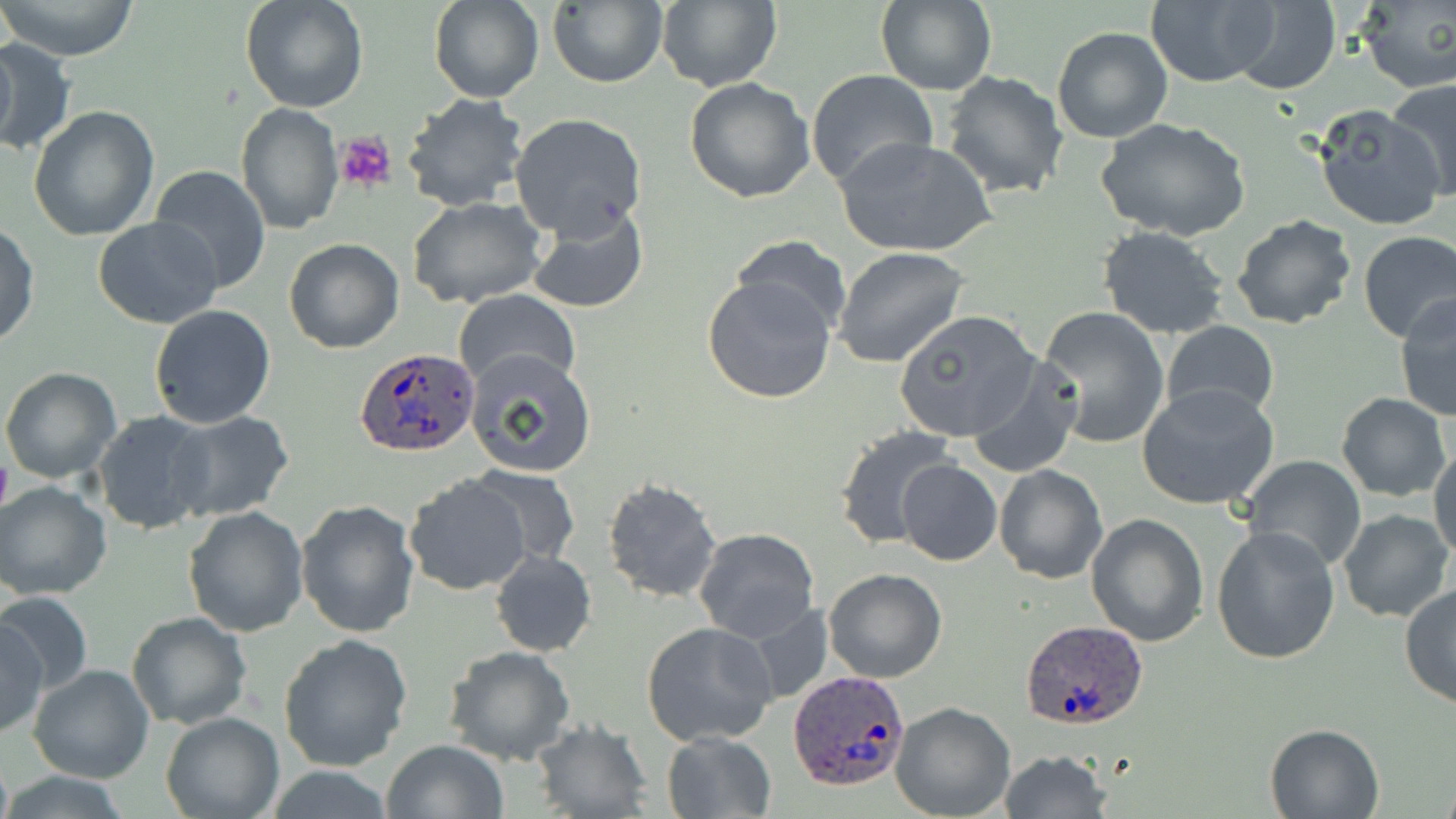

{
  "slide_level_diagnosis": "Plasmodium ovale",
  "magnification": "1000x",
  "uninfected_red_blood_cell_locations": "approximate bounding boxes as named x1/y1/x2/y2 corners in pixels: (x1=1, y1=0, x2=139, y2=61), (x1=239, y1=0, x2=368, y2=113), (x1=429, y1=0, x2=543, y2=103), (x1=547, y1=0, x2=668, y2=88), (x1=655, y1=0, x2=782, y2=92), (x1=1354, y1=0, x2=1456, y2=92), (x1=876, y1=1, x2=998, y2=97), (x1=1227, y1=1, x2=1341, y2=93), (x1=1143, y1=2, x2=1277, y2=87), (x1=1052, y1=26, x2=1173, y2=143), (x1=0, y1=37, x2=75, y2=159), (x1=805, y1=69, x2=938, y2=193), (x1=941, y1=70, x2=1070, y2=199), (x1=682, y1=77, x2=815, y2=204), (x1=1387, y1=78, x2=1456, y2=203), (x1=401, y1=93, x2=528, y2=211), (x1=236, y1=102, x2=344, y2=234), (x1=1310, y1=103, x2=1446, y2=231), (x1=29, y1=105, x2=160, y2=244), (x1=508, y1=112, x2=647, y2=239), (x1=1098, y1=120, x2=1249, y2=242), (x1=835, y1=135, x2=997, y2=259), (x1=149, y1=166, x2=272, y2=290), (x1=407, y1=197, x2=550, y2=309), (x1=525, y1=201, x2=650, y2=315), (x1=1231, y1=213, x2=1359, y2=331), (x1=94, y1=217, x2=222, y2=329), (x1=0, y1=223, x2=39, y2=348), (x1=1097, y1=226, x2=1230, y2=339), (x1=1356, y1=230, x2=1455, y2=342), (x1=732, y1=236, x2=851, y2=337), (x1=283, y1=238, x2=403, y2=354), (x1=832, y1=247, x2=967, y2=368), (x1=700, y1=273, x2=838, y2=405), (x1=453, y1=288, x2=580, y2=392), (x1=1393, y1=293, x2=1456, y2=422), (x1=148, y1=304, x2=277, y2=429), (x1=1036, y1=306, x2=1169, y2=450), (x1=893, y1=309, x2=1041, y2=443), (x1=1162, y1=321, x2=1280, y2=421), (x1=466, y1=350, x2=598, y2=478), (x1=966, y1=356, x2=1084, y2=477), (x1=0, y1=365, x2=122, y2=482), (x1=1138, y1=382, x2=1280, y2=511), (x1=1336, y1=393, x2=1452, y2=502), (x1=93, y1=411, x2=218, y2=535), (x1=166, y1=411, x2=295, y2=523), (x1=834, y1=425, x2=959, y2=549), (x1=1430, y1=442, x2=1456, y2=565), (x1=1240, y1=454, x2=1366, y2=572), (x1=896, y1=459, x2=1002, y2=566), (x1=994, y1=465, x2=1108, y2=584), (x1=464, y1=467, x2=582, y2=568), (x1=404, y1=475, x2=531, y2=594), (x1=600, y1=477, x2=723, y2=604), (x1=0, y1=480, x2=112, y2=600), (x1=296, y1=499, x2=420, y2=637), (x1=183, y1=505, x2=310, y2=635), (x1=1336, y1=507, x2=1453, y2=624), (x1=1086, y1=514, x2=1211, y2=646), (x1=1210, y1=524, x2=1342, y2=666), (x1=693, y1=527, x2=819, y2=643), (x1=490, y1=550, x2=597, y2=657), (x1=822, y1=567, x2=947, y2=682), (x1=1399, y1=582, x2=1456, y2=709), (x1=1, y1=590, x2=92, y2=696), (x1=126, y1=611, x2=254, y2=730), (x1=1, y1=617, x2=48, y2=738), (x1=641, y1=622, x2=778, y2=747), (x1=279, y1=633, x2=413, y2=771), (x1=443, y1=646, x2=574, y2=766), (x1=29, y1=664, x2=154, y2=783), (x1=890, y1=702, x2=1016, y2=819), (x1=160, y1=712, x2=285, y2=819), (x1=530, y1=720, x2=655, y2=817), (x1=1264, y1=722, x2=1386, y2=818), (x1=661, y1=731, x2=776, y2=818), (x1=381, y1=739, x2=510, y2=819), (x1=998, y1=750, x2=1111, y2=819), (x1=263, y1=766, x2=397, y2=819)",
  "field_of_view": "one of a larger specimen",
  "image_size": "1456×819 pixels",
  "platelet_locations": "approximate bounding boxes as named x1/y1/x2/y2 corners in pixels: (x1=335, y1=131, x2=397, y2=194)",
  "preparation": "thin blood smear",
  "plasmodium_ovale_infected_red_blood_cell_locations": "approximate bounding boxes as named x1/y1/x2/y2 corners in pixels: (x1=354, y1=346, x2=480, y2=457), (x1=1019, y1=620, x2=1149, y2=730), (x1=789, y1=670, x2=912, y2=791)",
  "modality": "optical microscopy",
  "stain": "May-Grünwald-Giemsa"
}